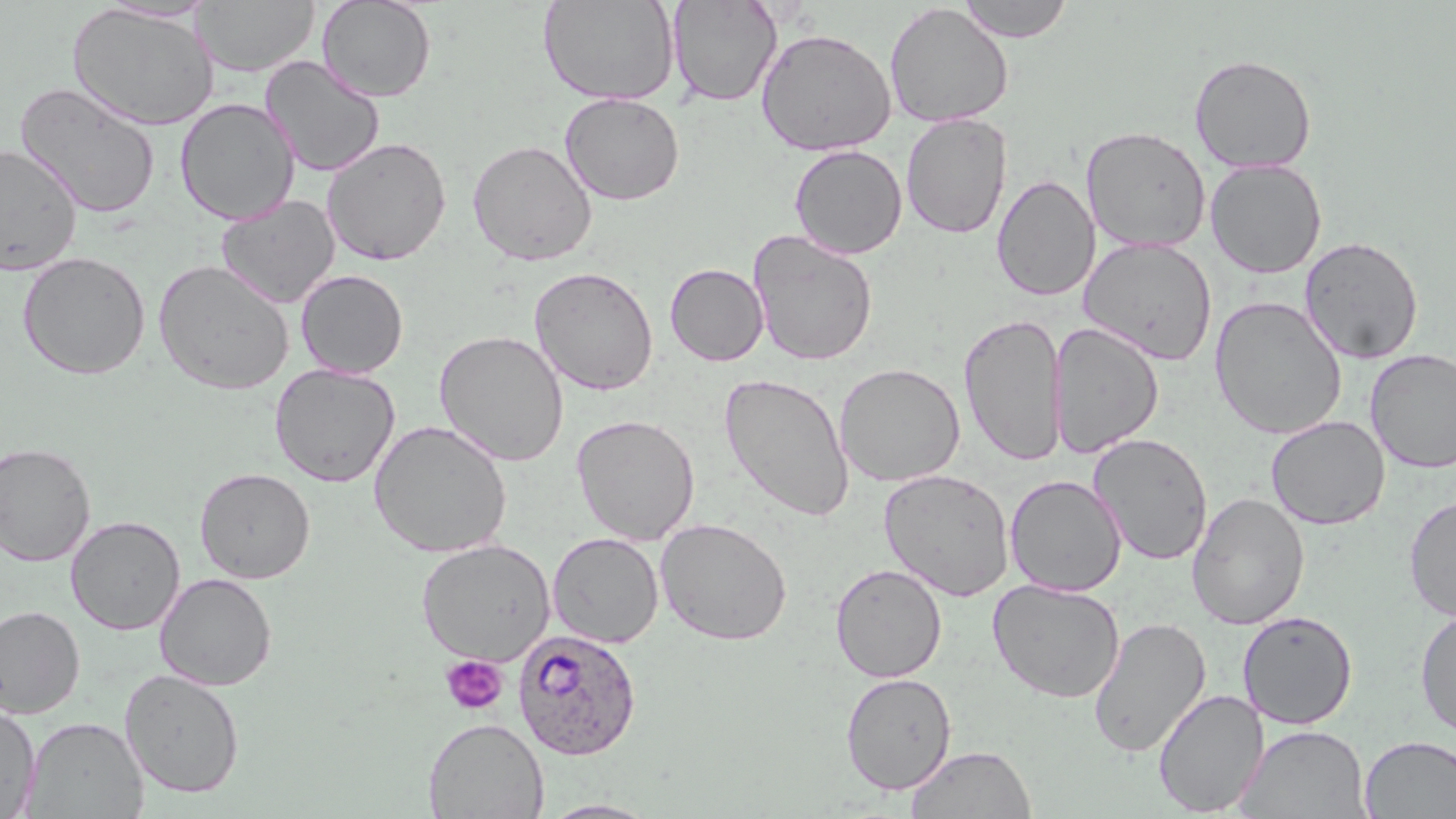

slide-level diagnosis = Plasmodium ovale
preparation = thin blood smear
magnification = 1000x
stain = May-Grünwald-Giemsa
image size = 1456×819 pixels
platelet locations = approximate bounding boxes as named x1/y1/x2/y2 corners in pixels: (x1=440, y1=654, x2=508, y2=715)
Plasmodium ovale-infected red blood cell locations = approximate bounding boxes as named x1/y1/x2/y2 corners in pixels: (x1=512, y1=627, x2=643, y2=760)
modality = optical microscopy
uninfected red blood cell locations = approximate bounding boxes as named x1/y1/x2/y2 corners in pixels: (x1=193, y1=0, x2=319, y2=76), (x1=316, y1=0, x2=436, y2=102), (x1=538, y1=0, x2=679, y2=105), (x1=668, y1=0, x2=782, y2=107), (x1=957, y1=0, x2=1075, y2=42), (x1=97, y1=1, x2=219, y2=23), (x1=66, y1=3, x2=220, y2=131), (x1=883, y1=3, x2=1014, y2=128), (x1=755, y1=27, x2=896, y2=157), (x1=1189, y1=54, x2=1317, y2=173), (x1=261, y1=55, x2=385, y2=176), (x1=15, y1=81, x2=162, y2=219), (x1=559, y1=92, x2=685, y2=206), (x1=175, y1=98, x2=299, y2=225), (x1=900, y1=113, x2=1012, y2=240), (x1=1081, y1=126, x2=1212, y2=252), (x1=322, y1=137, x2=451, y2=266), (x1=467, y1=139, x2=597, y2=266), (x1=789, y1=144, x2=908, y2=259), (x1=0, y1=145, x2=83, y2=276), (x1=1205, y1=159, x2=1327, y2=278), (x1=991, y1=174, x2=1099, y2=302), (x1=215, y1=194, x2=340, y2=309), (x1=748, y1=230, x2=878, y2=367), (x1=1079, y1=236, x2=1217, y2=365), (x1=1299, y1=236, x2=1424, y2=365), (x1=18, y1=251, x2=151, y2=380), (x1=153, y1=259, x2=294, y2=396), (x1=665, y1=263, x2=769, y2=366), (x1=529, y1=266, x2=659, y2=396), (x1=296, y1=270, x2=408, y2=378), (x1=1209, y1=296, x2=1347, y2=439), (x1=959, y1=313, x2=1067, y2=466), (x1=1049, y1=322, x2=1164, y2=459), (x1=434, y1=330, x2=569, y2=466), (x1=1365, y1=349, x2=1456, y2=473), (x1=835, y1=362, x2=965, y2=488), (x1=269, y1=364, x2=400, y2=487), (x1=719, y1=373, x2=855, y2=522), (x1=571, y1=414, x2=700, y2=545), (x1=1266, y1=415, x2=1390, y2=530), (x1=369, y1=420, x2=512, y2=558), (x1=1089, y1=432, x2=1213, y2=566), (x1=0, y1=442, x2=97, y2=566), (x1=194, y1=467, x2=315, y2=583), (x1=879, y1=468, x2=1014, y2=601), (x1=1005, y1=475, x2=1126, y2=597), (x1=1187, y1=492, x2=1310, y2=630), (x1=1403, y1=494, x2=1456, y2=621), (x1=65, y1=515, x2=185, y2=635), (x1=655, y1=517, x2=792, y2=645), (x1=548, y1=532, x2=663, y2=648), (x1=416, y1=538, x2=555, y2=666), (x1=830, y1=562, x2=947, y2=683), (x1=154, y1=572, x2=277, y2=691), (x1=987, y1=578, x2=1126, y2=703), (x1=0, y1=604, x2=85, y2=718), (x1=1415, y1=608, x2=1456, y2=739), (x1=1237, y1=610, x2=1358, y2=729), (x1=1087, y1=616, x2=1211, y2=758), (x1=119, y1=668, x2=245, y2=798), (x1=840, y1=672, x2=956, y2=794), (x1=1153, y1=688, x2=1269, y2=816), (x1=0, y1=701, x2=41, y2=818), (x1=23, y1=716, x2=149, y2=818), (x1=422, y1=717, x2=548, y2=819), (x1=1236, y1=724, x2=1371, y2=819), (x1=1359, y1=735, x2=1456, y2=818), (x1=906, y1=745, x2=1036, y2=819), (x1=537, y1=799, x2=663, y2=818)
field of view = one of a larger specimen